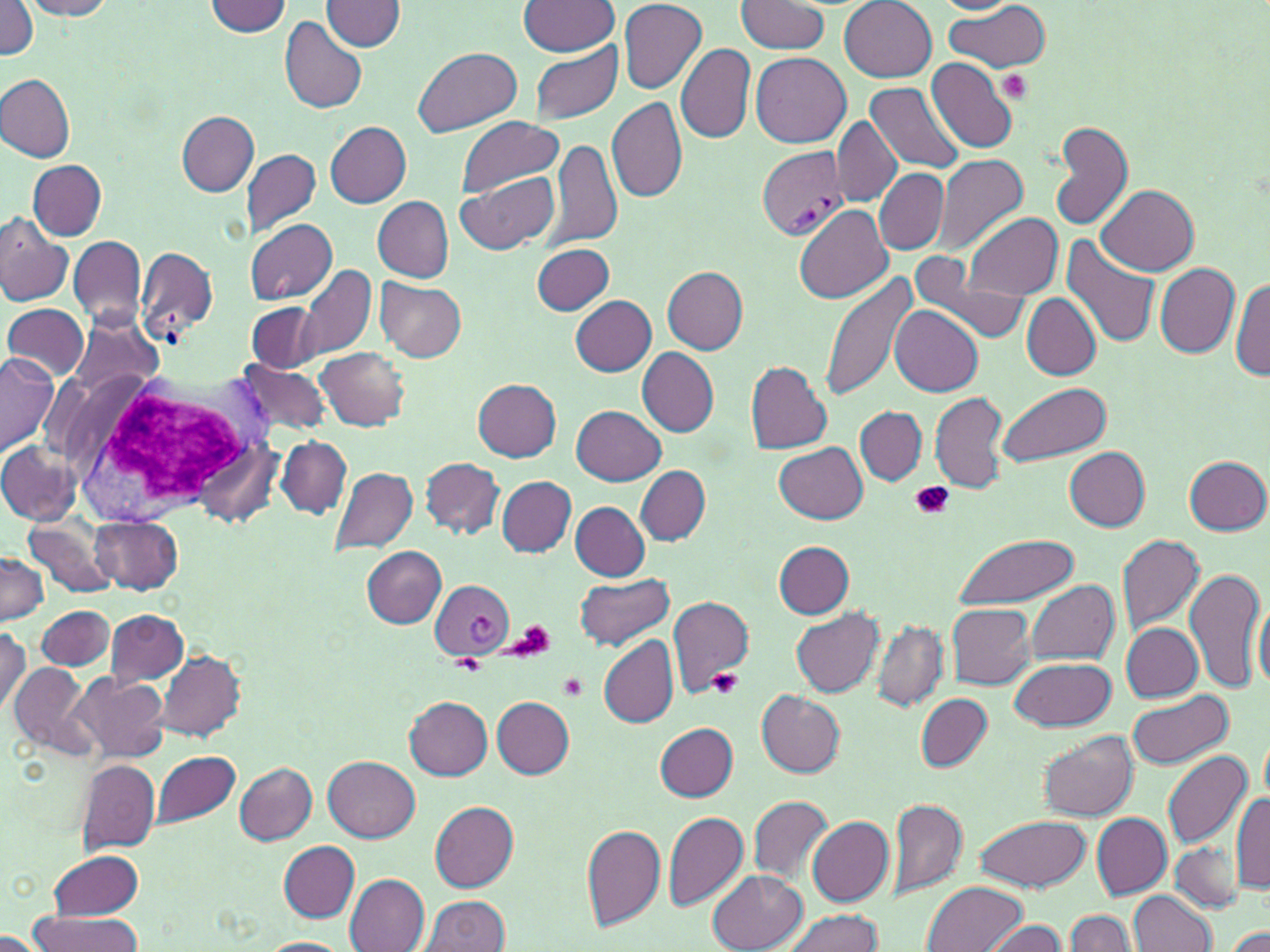

slide-level diagnosis = Plasmodium vivax
magnification = 1000x
stain = May-Grünwald-Giemsa
white blood cell locations = approximate bounding boxes as named x1/y1/x2/y2 corners in pixels: (x1=52, y1=367, x2=271, y2=527)
modality = light microscopy
preparation = thin blood film
Plasmodium vivax-infected red blood cell locations = approximate bounding boxes as named x1/y1/x2/y2 corners in pixels: (x1=757, y1=145, x2=849, y2=241), (x1=431, y1=580, x2=515, y2=658)
field of view = one of a larger specimen
image size = 1270×952 pixels
uninfected red blood cell locations = approximate bounding boxes as named x1/y1/x2/y2 corners in pixels: (x1=22, y1=0, x2=118, y2=18), (x1=322, y1=0, x2=406, y2=51), (x1=839, y1=0, x2=937, y2=82), (x1=0, y1=1, x2=39, y2=58), (x1=205, y1=1, x2=293, y2=36), (x1=520, y1=1, x2=619, y2=56), (x1=619, y1=1, x2=706, y2=93), (x1=933, y1=1, x2=1020, y2=14), (x1=736, y1=2, x2=829, y2=52), (x1=942, y1=4, x2=1052, y2=73), (x1=279, y1=17, x2=368, y2=114), (x1=528, y1=41, x2=622, y2=124), (x1=677, y1=43, x2=755, y2=145), (x1=414, y1=47, x2=521, y2=137), (x1=752, y1=53, x2=851, y2=148), (x1=927, y1=57, x2=1019, y2=153), (x1=1, y1=74, x2=75, y2=162), (x1=867, y1=82, x2=966, y2=174), (x1=605, y1=97, x2=688, y2=203), (x1=177, y1=112, x2=257, y2=195), (x1=455, y1=117, x2=562, y2=199), (x1=832, y1=117, x2=900, y2=206), (x1=1050, y1=121, x2=1134, y2=231), (x1=327, y1=122, x2=411, y2=207), (x1=550, y1=140, x2=623, y2=251), (x1=241, y1=147, x2=322, y2=237), (x1=932, y1=153, x2=1029, y2=255), (x1=28, y1=160, x2=106, y2=239), (x1=875, y1=168, x2=948, y2=254), (x1=456, y1=170, x2=559, y2=255), (x1=1098, y1=185, x2=1198, y2=276), (x1=374, y1=197, x2=454, y2=282), (x1=794, y1=204, x2=892, y2=303), (x1=963, y1=212, x2=1062, y2=300), (x1=0, y1=218, x2=74, y2=306), (x1=246, y1=219, x2=338, y2=305), (x1=69, y1=234, x2=147, y2=331), (x1=1062, y1=235, x2=1161, y2=348), (x1=136, y1=245, x2=217, y2=344), (x1=532, y1=245, x2=615, y2=314), (x1=909, y1=251, x2=1030, y2=344), (x1=1155, y1=263, x2=1239, y2=357), (x1=300, y1=264, x2=375, y2=359), (x1=662, y1=266, x2=748, y2=354), (x1=820, y1=271, x2=921, y2=404), (x1=1232, y1=276, x2=1270, y2=381), (x1=376, y1=279, x2=467, y2=362), (x1=1022, y1=293, x2=1100, y2=380), (x1=570, y1=296, x2=657, y2=375), (x1=248, y1=302, x2=322, y2=373), (x1=2, y1=304, x2=88, y2=383), (x1=891, y1=305, x2=981, y2=396), (x1=70, y1=315, x2=163, y2=401), (x1=316, y1=346, x2=410, y2=430), (x1=637, y1=347, x2=719, y2=437), (x1=0, y1=353, x2=58, y2=457), (x1=235, y1=358, x2=333, y2=439), (x1=745, y1=361, x2=832, y2=453), (x1=473, y1=378, x2=562, y2=460), (x1=995, y1=382, x2=1109, y2=468), (x1=930, y1=390, x2=1007, y2=494), (x1=572, y1=406, x2=666, y2=485), (x1=856, y1=407, x2=927, y2=485), (x1=277, y1=438, x2=350, y2=517), (x1=195, y1=441, x2=281, y2=528), (x1=0, y1=442, x2=83, y2=523), (x1=776, y1=442, x2=867, y2=524), (x1=1064, y1=446, x2=1150, y2=530), (x1=1185, y1=456, x2=1269, y2=535), (x1=421, y1=458, x2=503, y2=537), (x1=636, y1=465, x2=709, y2=544), (x1=329, y1=466, x2=419, y2=556), (x1=497, y1=477, x2=576, y2=556), (x1=571, y1=502, x2=650, y2=579), (x1=89, y1=514, x2=183, y2=593), (x1=26, y1=518, x2=119, y2=597), (x1=953, y1=533, x2=1080, y2=608), (x1=1117, y1=533, x2=1205, y2=634), (x1=775, y1=541, x2=853, y2=618), (x1=361, y1=545, x2=446, y2=627), (x1=0, y1=552, x2=48, y2=625), (x1=1184, y1=567, x2=1265, y2=694), (x1=575, y1=574, x2=674, y2=650), (x1=1026, y1=580, x2=1119, y2=665), (x1=666, y1=595, x2=754, y2=694), (x1=1254, y1=595, x2=1270, y2=691), (x1=947, y1=603, x2=1036, y2=689), (x1=36, y1=606, x2=115, y2=671), (x1=791, y1=607, x2=884, y2=697), (x1=107, y1=610, x2=188, y2=687), (x1=873, y1=621, x2=947, y2=710), (x1=1122, y1=623, x2=1205, y2=701), (x1=0, y1=625, x2=30, y2=719), (x1=599, y1=632, x2=679, y2=726), (x1=151, y1=650, x2=247, y2=744), (x1=1010, y1=656, x2=1116, y2=731), (x1=9, y1=662, x2=92, y2=756), (x1=70, y1=674, x2=170, y2=763), (x1=757, y1=691, x2=844, y2=777), (x1=1126, y1=691, x2=1233, y2=770), (x1=915, y1=694, x2=992, y2=772), (x1=405, y1=696, x2=493, y2=779), (x1=492, y1=696, x2=573, y2=777), (x1=656, y1=723, x2=737, y2=800), (x1=1038, y1=731, x2=1139, y2=821), (x1=1161, y1=751, x2=1254, y2=848), (x1=151, y1=752, x2=240, y2=827), (x1=325, y1=756, x2=419, y2=841), (x1=75, y1=758, x2=160, y2=855), (x1=236, y1=762, x2=316, y2=845), (x1=750, y1=794, x2=832, y2=887), (x1=1232, y1=794, x2=1270, y2=893), (x1=887, y1=796, x2=967, y2=899), (x1=429, y1=800, x2=519, y2=891), (x1=661, y1=811, x2=750, y2=913), (x1=1091, y1=813, x2=1171, y2=898), (x1=975, y1=815, x2=1090, y2=892), (x1=807, y1=816, x2=893, y2=907), (x1=577, y1=819, x2=752, y2=924), (x1=581, y1=824, x2=666, y2=932), (x1=279, y1=840, x2=359, y2=923), (x1=1171, y1=842, x2=1243, y2=911), (x1=49, y1=849, x2=143, y2=920), (x1=708, y1=870, x2=807, y2=952), (x1=344, y1=873, x2=430, y2=952), (x1=923, y1=881, x2=1025, y2=951), (x1=1129, y1=890, x2=1215, y2=951), (x1=421, y1=895, x2=510, y2=951), (x1=778, y1=908, x2=883, y2=952), (x1=1065, y1=910, x2=1135, y2=952), (x1=27, y1=912, x2=147, y2=951), (x1=983, y1=919, x2=1070, y2=952), (x1=1228, y1=926, x2=1270, y2=951), (x1=1, y1=931, x2=48, y2=951), (x1=259, y1=937, x2=350, y2=952)
platelet locations = approximate bounding boxes as named x1/y1/x2/y2 corners in pixels: (x1=998, y1=70, x2=1032, y2=103), (x1=913, y1=482, x2=952, y2=519), (x1=504, y1=622, x2=556, y2=662), (x1=451, y1=658, x2=486, y2=674), (x1=707, y1=669, x2=744, y2=699), (x1=560, y1=673, x2=588, y2=701)